Point out every malaria parasite and every leukocyte.
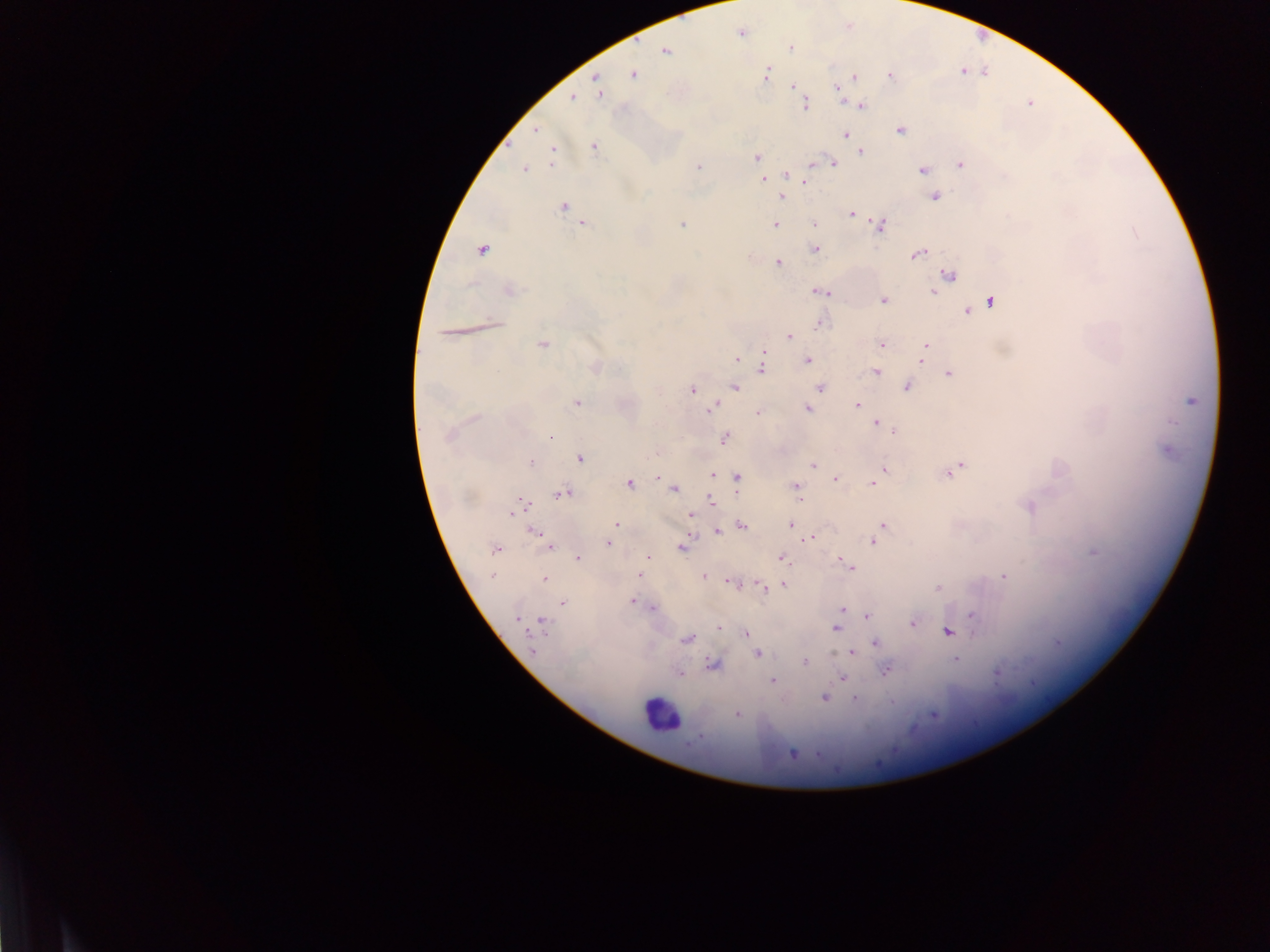
Approximate centers as x y in pixels.
Malaria parasites: 741 33; 791 48; 665 50; 963 72; 633 74; 767 74; 889 76; 853 78; 596 80; 793 86; 597 87; 837 88; 573 98; 805 105; 860 105; 536 130; 901 130; 845 135; 594 147; 860 151; 552 154; 756 157; 815 163; 832 164; 960 164; 699 167; 524 169; 922 170; 786 175; 763 180; 804 181; 782 197; 934 197; 563 207; 851 214; 814 223; 584 224; 682 225; 775 225; 879 225; 1134 231; 816 249; 481 250; 917 254; 778 263; 949 276; 510 290; 822 291; 933 291; 883 301; 990 302; 968 311; 493 323; 821 324; 449 333; 788 336; 543 344; 882 344; 925 347; 738 358; 807 360; 922 360; 595 367; 762 368; 876 372; 949 373; 735 387; 821 388; 907 388; 692 390; 1191 401; 576 404; 857 405; 712 407; 807 409; 757 412; 475 419; 877 423; 893 432; 448 436; 550 436; 725 438; 1167 451; 580 459; 532 462; 814 465; 959 466; 884 469; 954 471; 712 475; 657 477; 738 478; 836 478; 629 484; 873 484; 795 486; 674 489; 562 493; 712 502; 518 507; 1028 507; 691 516; 790 524; 616 525; 744 526; 884 526; 718 531; 534 533; 811 538; 873 541; 607 542; 549 546; 681 547; 495 549; 1093 552; 648 557; 578 558; 782 559; 849 565; 492 576; 639 576; 704 576; 1003 577; 545 579; 732 583; 784 585; 762 587; 938 588; 632 602; 562 603; 653 608; 842 609; 867 615; 973 616; 517 619; 543 622; 912 623; 719 626; 836 628; 948 631; 746 633; 687 639; 875 643; 1057 643; 533 650; 852 652; 757 653; 955 659; 805 662; 714 664; 886 671; 680 673; 997 674; 842 677; 772 682; 824 698; 855 698; 737 714; 792 753.
Leukocytes: 660 714.

capture: mobile-phone photograph through a microscope
field_of_view: single
image_size: 1270×952 pixels
country: Ghana
preparation: thick blood smear